Report the malaria status of this cell.
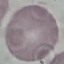
It is uninfected.

Summary:
  - Image type: automatically extracted cell patch, resized to 64 × 64 pixels
  - Preparation: thin smear
  - Capture: smartphone camera at the microscope eyepiece
  - Stain: Giemsa